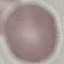 Result: no malaria parasites detected. Cell patch, automatically extracted from a larger field of view and resized to 64 × 64 pixels. Giemsa stain. Thin blood film. Photographed with a smartphone camera at the microscope eyepiece.